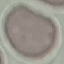
Malaria status: uninfected. Acquired by smartphone through the microscope eyepiece. Thin smear of blood. Giemsa-stained preparation. Automatically extracted cell patch, resized to 64 × 64 pixels.